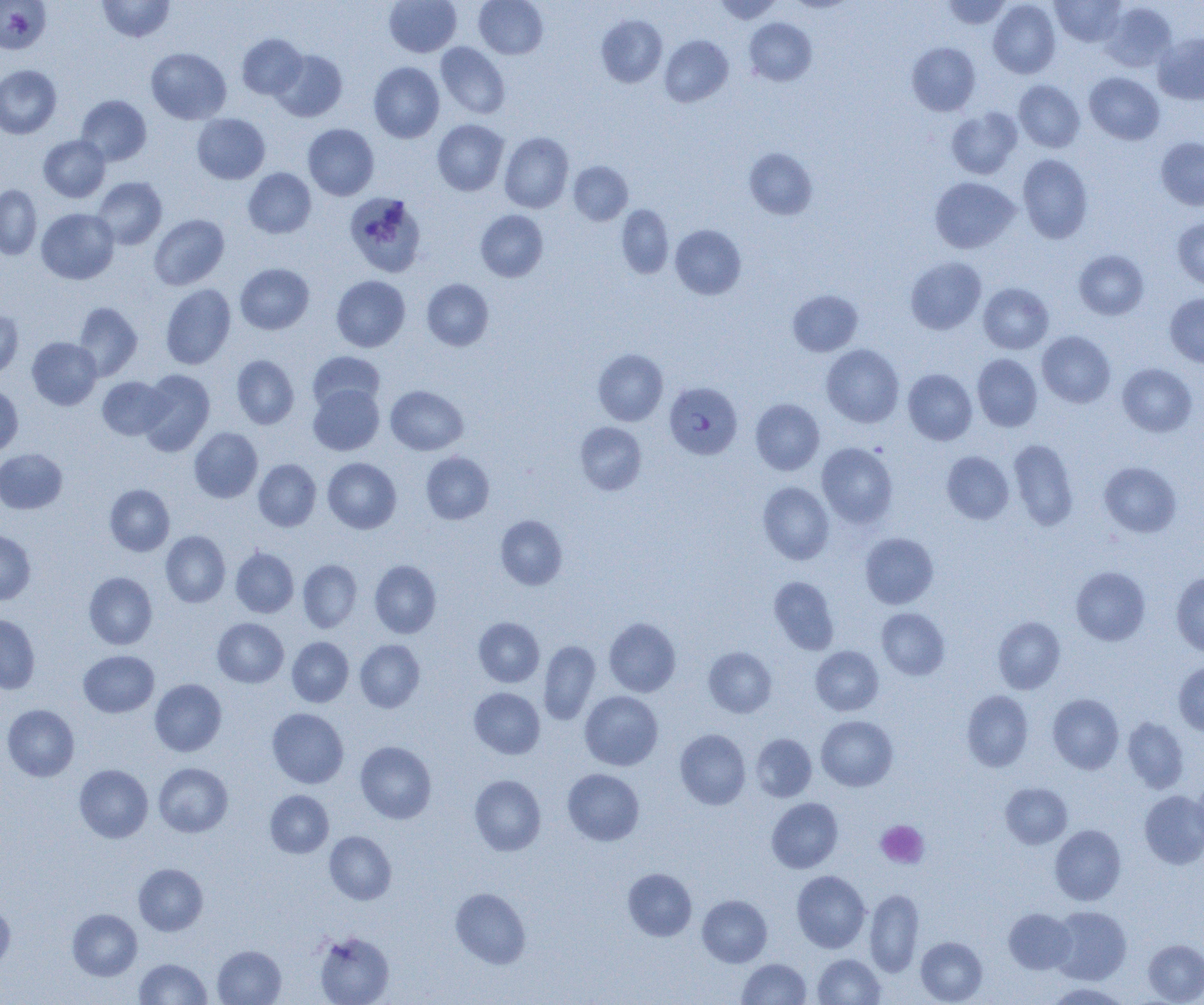
Approximate bounding boxes as named x1/y1/x2/y2 corners in pixels. Platelet locations: (x1=876, y1=820, x2=929, y2=868). Plasmodium falciparum-infected red blood cell locations: (x1=664, y1=381, x2=742, y2=459). Uninfected red blood cell locations: (x1=0, y1=0, x2=50, y2=54), (x1=97, y1=0, x2=175, y2=42), (x1=385, y1=0, x2=461, y2=57), (x1=474, y1=0, x2=547, y2=59), (x1=715, y1=0, x2=782, y2=24), (x1=942, y1=0, x2=1012, y2=29), (x1=1051, y1=0, x2=1127, y2=47), (x1=989, y1=1, x2=1060, y2=78), (x1=1101, y1=2, x2=1176, y2=72), (x1=596, y1=15, x2=667, y2=87), (x1=745, y1=18, x2=816, y2=85), (x1=1153, y1=33, x2=1204, y2=105), (x1=237, y1=34, x2=307, y2=99), (x1=660, y1=35, x2=733, y2=106), (x1=436, y1=42, x2=510, y2=119), (x1=907, y1=42, x2=980, y2=115), (x1=146, y1=48, x2=231, y2=124), (x1=272, y1=50, x2=347, y2=122), (x1=368, y1=62, x2=444, y2=143), (x1=0, y1=64, x2=61, y2=139), (x1=1084, y1=72, x2=1164, y2=144), (x1=1014, y1=80, x2=1084, y2=152), (x1=76, y1=95, x2=151, y2=165), (x1=946, y1=108, x2=1022, y2=179), (x1=192, y1=113, x2=270, y2=184), (x1=432, y1=119, x2=509, y2=195), (x1=303, y1=124, x2=379, y2=200), (x1=499, y1=132, x2=573, y2=213), (x1=39, y1=135, x2=110, y2=202), (x1=1156, y1=137, x2=1204, y2=210), (x1=744, y1=148, x2=817, y2=219), (x1=1017, y1=154, x2=1093, y2=243), (x1=568, y1=161, x2=633, y2=225), (x1=243, y1=168, x2=316, y2=238), (x1=92, y1=177, x2=167, y2=249), (x1=930, y1=177, x2=1019, y2=253), (x1=0, y1=184, x2=42, y2=259), (x1=344, y1=192, x2=426, y2=277), (x1=616, y1=204, x2=673, y2=279), (x1=36, y1=208, x2=119, y2=284), (x1=476, y1=210, x2=548, y2=281), (x1=149, y1=214, x2=229, y2=290), (x1=1172, y1=218, x2=1204, y2=289), (x1=670, y1=225, x2=746, y2=299), (x1=1074, y1=249, x2=1149, y2=320), (x1=905, y1=257, x2=986, y2=334), (x1=236, y1=263, x2=314, y2=334), (x1=331, y1=275, x2=410, y2=352), (x1=422, y1=279, x2=493, y2=351), (x1=978, y1=283, x2=1053, y2=353), (x1=161, y1=284, x2=236, y2=369), (x1=788, y1=290, x2=862, y2=356), (x1=1165, y1=293, x2=1204, y2=368), (x1=73, y1=302, x2=142, y2=380), (x1=0, y1=310, x2=23, y2=381), (x1=1037, y1=331, x2=1115, y2=407), (x1=27, y1=337, x2=102, y2=410), (x1=821, y1=344, x2=904, y2=427), (x1=593, y1=349, x2=668, y2=426), (x1=308, y1=351, x2=384, y2=413), (x1=972, y1=354, x2=1042, y2=431), (x1=232, y1=355, x2=299, y2=429), (x1=1117, y1=363, x2=1198, y2=437), (x1=138, y1=369, x2=214, y2=456), (x1=903, y1=369, x2=977, y2=444), (x1=97, y1=377, x2=172, y2=440), (x1=308, y1=384, x2=384, y2=455), (x1=0, y1=385, x2=23, y2=455), (x1=386, y1=385, x2=468, y2=455), (x1=751, y1=399, x2=824, y2=474), (x1=575, y1=422, x2=647, y2=495), (x1=189, y1=427, x2=262, y2=503), (x1=1009, y1=439, x2=1079, y2=530), (x1=817, y1=442, x2=898, y2=528), (x1=0, y1=448, x2=67, y2=514), (x1=942, y1=450, x2=1014, y2=524), (x1=421, y1=452, x2=494, y2=524), (x1=323, y1=457, x2=401, y2=533), (x1=253, y1=459, x2=321, y2=531), (x1=1099, y1=461, x2=1181, y2=537), (x1=758, y1=482, x2=834, y2=564), (x1=105, y1=484, x2=175, y2=556), (x1=495, y1=515, x2=567, y2=590), (x1=0, y1=530, x2=36, y2=604), (x1=161, y1=531, x2=230, y2=607), (x1=860, y1=532, x2=938, y2=609), (x1=231, y1=547, x2=299, y2=617), (x1=297, y1=560, x2=362, y2=632), (x1=369, y1=560, x2=441, y2=638), (x1=1071, y1=566, x2=1150, y2=645), (x1=84, y1=572, x2=157, y2=649), (x1=1170, y1=572, x2=1204, y2=655), (x1=769, y1=576, x2=839, y2=654), (x1=876, y1=607, x2=950, y2=679), (x1=0, y1=614, x2=40, y2=694), (x1=993, y1=616, x2=1065, y2=693), (x1=474, y1=617, x2=544, y2=687), (x1=212, y1=618, x2=288, y2=687), (x1=604, y1=618, x2=680, y2=697), (x1=287, y1=637, x2=353, y2=707), (x1=355, y1=639, x2=425, y2=712), (x1=539, y1=640, x2=600, y2=724), (x1=810, y1=646, x2=883, y2=716), (x1=704, y1=647, x2=776, y2=717), (x1=79, y1=650, x2=159, y2=717), (x1=1173, y1=662, x2=1204, y2=736), (x1=150, y1=679, x2=227, y2=757), (x1=469, y1=687, x2=545, y2=758), (x1=961, y1=690, x2=1033, y2=771), (x1=580, y1=691, x2=663, y2=770), (x1=1048, y1=694, x2=1124, y2=773), (x1=2, y1=704, x2=79, y2=781), (x1=267, y1=708, x2=348, y2=788), (x1=816, y1=715, x2=898, y2=791), (x1=1123, y1=717, x2=1189, y2=792), (x1=675, y1=729, x2=751, y2=810), (x1=751, y1=734, x2=817, y2=802), (x1=355, y1=741, x2=436, y2=823), (x1=154, y1=763, x2=233, y2=837), (x1=74, y1=764, x2=153, y2=842), (x1=562, y1=768, x2=644, y2=845), (x1=469, y1=774, x2=546, y2=856), (x1=1192, y1=778, x2=1204, y2=848), (x1=1001, y1=782, x2=1072, y2=849), (x1=265, y1=790, x2=334, y2=858), (x1=1139, y1=790, x2=1204, y2=869), (x1=767, y1=798, x2=843, y2=873), (x1=1050, y1=825, x2=1126, y2=905), (x1=325, y1=831, x2=396, y2=904), (x1=134, y1=863, x2=208, y2=935), (x1=623, y1=868, x2=696, y2=941), (x1=791, y1=870, x2=870, y2=953), (x1=451, y1=887, x2=531, y2=969), (x1=864, y1=889, x2=924, y2=977), (x1=697, y1=895, x2=772, y2=967), (x1=0, y1=902, x2=15, y2=972), (x1=1049, y1=906, x2=1131, y2=985), (x1=1003, y1=908, x2=1076, y2=973), (x1=68, y1=909, x2=142, y2=980), (x1=314, y1=931, x2=395, y2=1005), (x1=916, y1=937, x2=987, y2=1004), (x1=1143, y1=939, x2=1204, y2=1004), (x1=213, y1=945, x2=286, y2=1004), (x1=813, y1=953, x2=885, y2=1004), (x1=134, y1=957, x2=211, y2=1005), (x1=737, y1=958, x2=811, y2=1004), (x1=1046, y1=982, x2=1130, y2=1004). Slide-level diagnosis: Plasmodium falciparum. Optical microscopy. Single field of view. Image is 1204×1005 pixels. 1000x magnification. Thin blood smear.